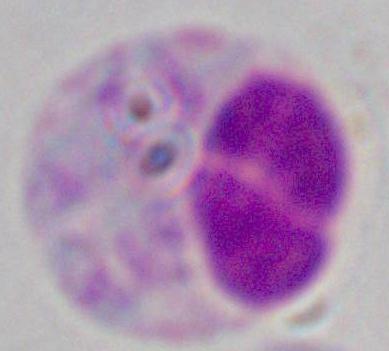 Captured at 1000x magnification. A white blood cell is seen. Micrograph.